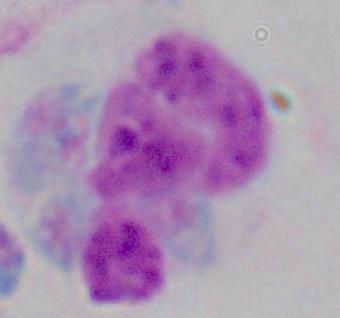

identification = leukocyte
modality = micrograph
magnification = 1000x